Point out malaria parasites and leukocytes.
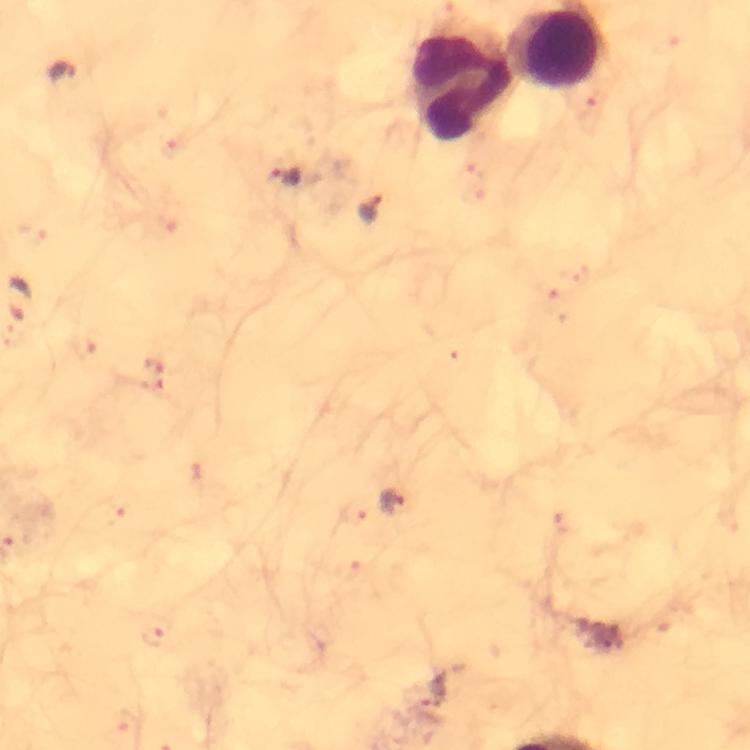

Approximate centers as [x, y] in pixels.
Malaria parasites: [60, 72], [173, 148], [284, 178], [370, 208], [21, 298], [84, 348], [196, 473], [389, 502], [112, 513], [353, 514], [153, 632], [127, 719].
Leukocytes: [554, 48], [464, 85].

{
  "cropped_from": "one field of view",
  "context": "from a malaria diagnostic workup",
  "image_size": "750×750 pixels",
  "capture": "smartphone mounted on the microscope",
  "magnification": "100x",
  "preparation": "thick smear",
  "immersion_oil": "used",
  "stain": "Giemsa"
}